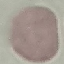
Summary:
  - Malaria status: uninfected
  - Preparation: thin blood film
  - Image type: cell patch, automatically extracted from a larger field of view and resized to 64 × 64 pixels
  - Capture: smartphone camera at the microscope eyepiece
  - Stain: Giemsa